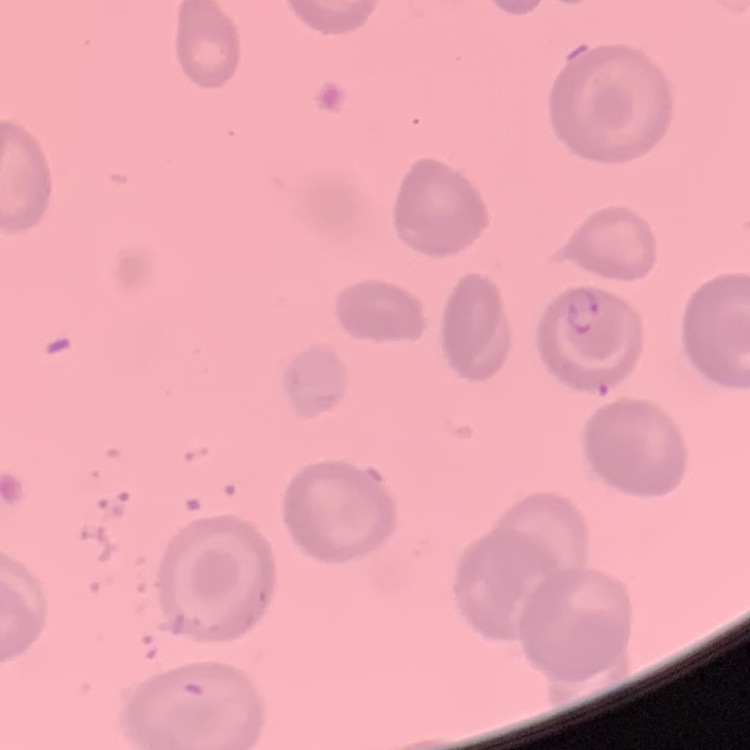
{
  "erythrocyte_morphology": "no rouleaux formation",
  "preparation": "thin peripheral smear",
  "stain": "Field's or Giemsa",
  "image_type": "one tile cut from a larger photomicrograph"
}